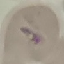

malaria status = parasitized
stain = Giemsa
preparation = thin smear
capture = smartphone camera at the microscope eyepiece
image type = automatically extracted cell patch, resized to 64 × 64 pixels